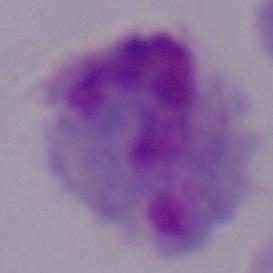
modality = micrograph
magnification = 1000x
identification = trichomonad